Identify the cell.
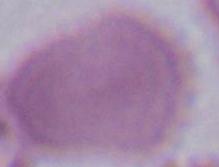
This is an erythrocyte.

{
  "magnification": "1000x",
  "modality": "photomicrograph"
}